Locate and identify every blood parasite.
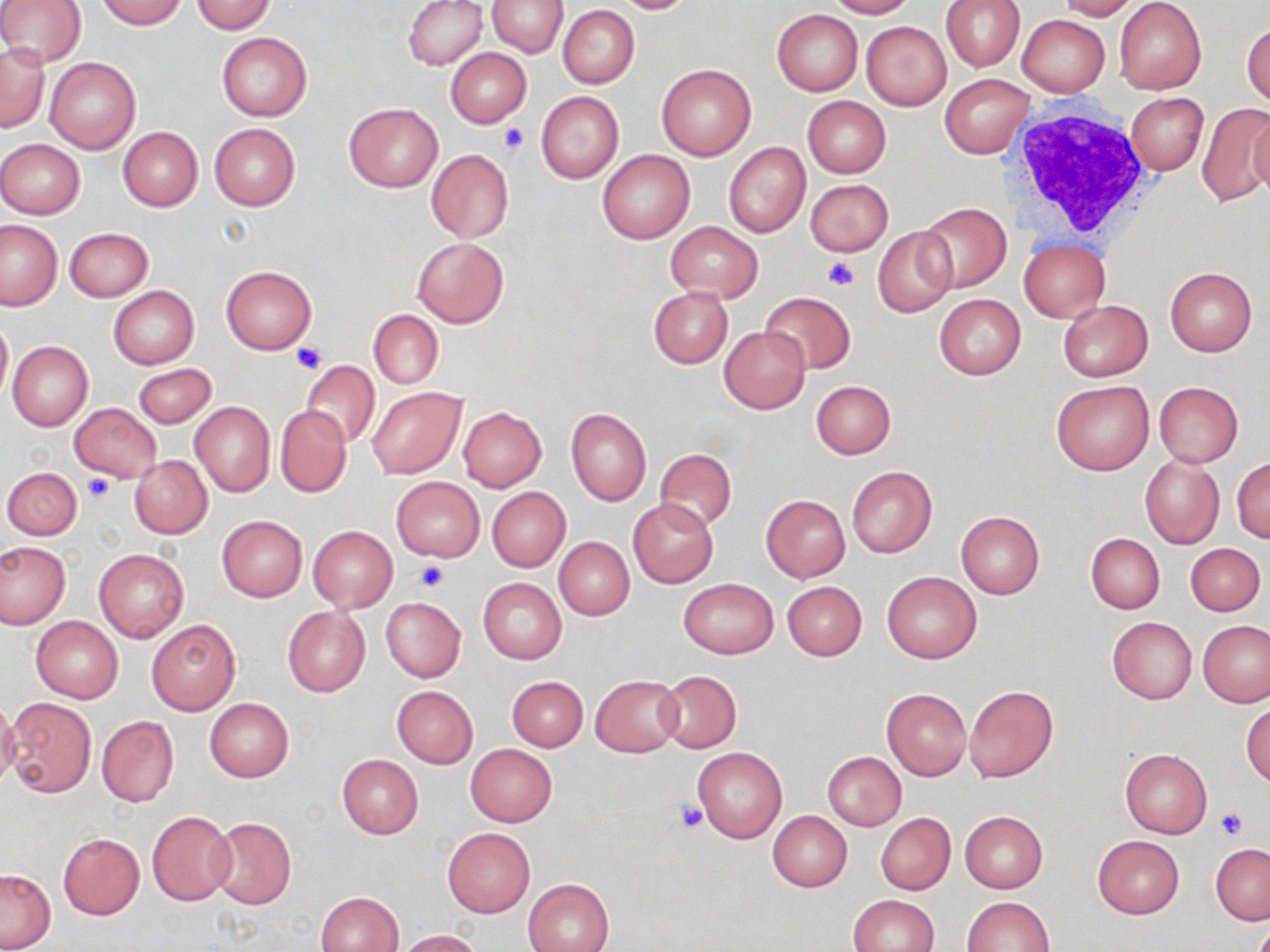
No blood parasites seen.

Approximate bounding boxes as (x1, y1, x2, y2) in pixels. Platelet locations: (499, 123, 527, 156), (821, 255, 858, 290), (291, 344, 325, 375), (84, 472, 115, 503), (415, 560, 448, 591), (674, 800, 708, 834), (1218, 808, 1246, 838). Uninfected red blood cell locations: (0, 0, 86, 66), (95, 0, 186, 29), (403, 0, 487, 70), (487, 0, 568, 57), (609, 0, 700, 15), (824, 0, 914, 18), (940, 0, 1024, 72), (1055, 0, 1140, 20), (1114, 0, 1206, 95), (191, 1, 277, 33), (558, 6, 639, 89), (772, 10, 862, 95), (1016, 15, 1110, 97), (1243, 20, 1270, 106), (861, 21, 950, 109), (216, 33, 312, 121), (0, 43, 49, 133), (445, 48, 531, 128), (45, 57, 140, 154), (656, 63, 755, 160), (939, 74, 1033, 159), (535, 90, 624, 184), (1126, 92, 1209, 176), (802, 96, 890, 177), (343, 102, 442, 192), (1197, 103, 1268, 206), (1248, 112, 1270, 199), (210, 123, 300, 211), (117, 127, 202, 211), (0, 139, 86, 219), (724, 143, 810, 237), (597, 147, 694, 244), (426, 148, 514, 243), (804, 179, 893, 256), (916, 202, 1011, 294), (1, 220, 63, 311), (666, 221, 762, 301), (656, 224, 749, 367), (872, 226, 956, 319), (64, 227, 154, 301), (413, 237, 508, 328), (1018, 239, 1110, 323), (220, 266, 316, 354), (1165, 268, 1257, 356), (108, 286, 199, 368), (648, 286, 733, 368), (762, 291, 855, 374), (934, 295, 1026, 380), (1058, 300, 1153, 382), (369, 310, 444, 388), (0, 314, 12, 409), (719, 326, 809, 412), (7, 340, 93, 430), (301, 360, 380, 449), (132, 363, 216, 428), (812, 380, 896, 459), (1051, 381, 1154, 476), (1154, 381, 1244, 467), (366, 387, 466, 479), (189, 401, 275, 497), (70, 403, 161, 483), (275, 405, 352, 498), (458, 406, 547, 491), (566, 408, 651, 505), (657, 449, 735, 530), (1139, 454, 1224, 549), (130, 456, 213, 538), (1231, 457, 1270, 543), (846, 465, 936, 558), (3, 467, 81, 539), (391, 477, 484, 561), (486, 487, 569, 572), (761, 495, 850, 581), (627, 498, 718, 589), (956, 511, 1045, 599), (217, 515, 307, 602), (309, 526, 397, 612), (1086, 533, 1164, 614), (553, 536, 634, 620), (0, 542, 69, 628), (1185, 543, 1266, 615), (94, 549, 189, 643), (881, 571, 981, 664), (478, 578, 567, 664), (679, 578, 778, 659), (783, 582, 867, 661), (381, 597, 466, 682), (282, 607, 371, 698), (31, 616, 123, 703), (1106, 617, 1196, 704), (147, 619, 240, 715), (1198, 621, 1270, 707), (657, 671, 741, 752), (591, 675, 682, 757), (507, 676, 588, 753), (964, 685, 1058, 783), (392, 686, 478, 767), (882, 688, 972, 780), (5, 698, 95, 797), (204, 698, 294, 782), (1242, 700, 1270, 787), (0, 701, 20, 789), (96, 716, 178, 806), (465, 744, 558, 827), (692, 747, 787, 844), (1119, 748, 1211, 839), (823, 752, 905, 830), (336, 754, 423, 839), (767, 811, 852, 892), (959, 811, 1047, 893), (146, 812, 236, 905), (876, 813, 955, 894), (207, 816, 296, 911), (441, 828, 535, 917), (58, 833, 144, 920), (1092, 835, 1185, 919), (1211, 845, 1270, 924), (0, 868, 56, 950), (522, 878, 613, 952), (316, 890, 404, 952), (848, 895, 939, 952), (962, 897, 1055, 951), (393, 929, 484, 951). White blood cell locations: (1009, 106, 1153, 240). Slide-level diagnosis: negative for blood parasites. Captured at 1000x magnification. Thin blood film. Image is 1270×952 pixels. One field of a larger specimen. Optical microscopy. May-Grünwald-Giemsa-stained preparation.